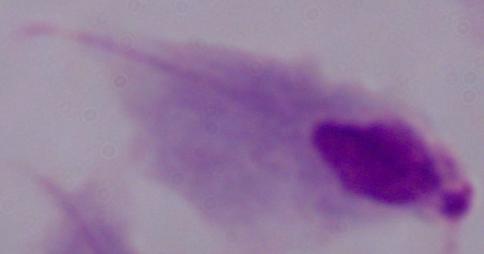

A trichomonad is seen. 1000x magnification. Micrograph.